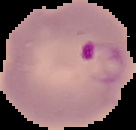
Image is 136×130 pixels. The area outside the segmented cell region is set to black. Result: malaria parasites identified. From a thin blood smear.